Assess this cell for malaria.
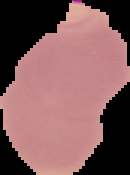
Parasitized.

{
  "preparation": "thin blood smear",
  "image_type": "segmented cell region with the area outside set to black",
  "image_size": "130×175 pixels"
}